Identify the blood parasite species.
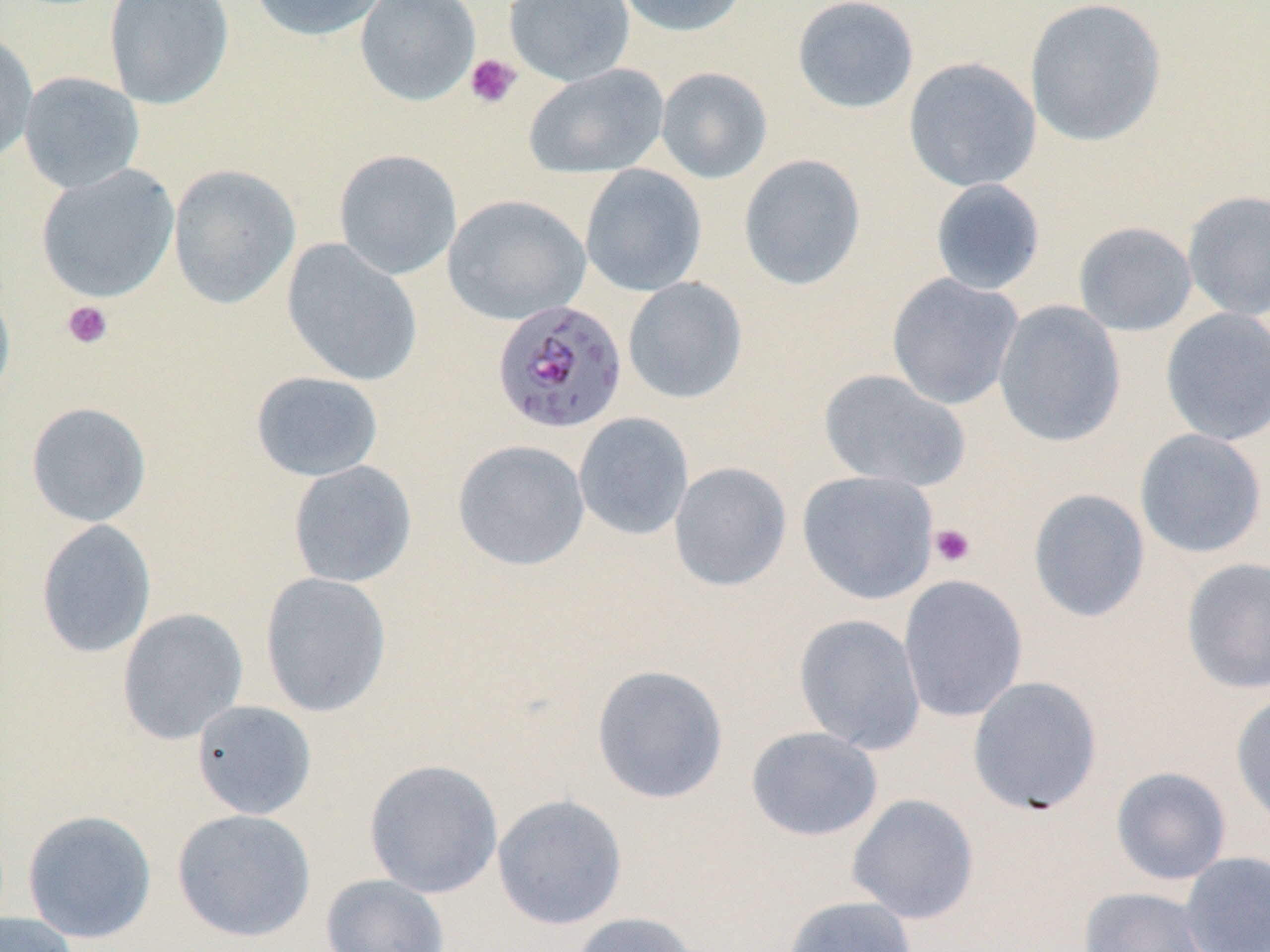

Plasmodium falciparum.

Summary:
  - Coordinate format: approximate bounding boxes as (x1, y1, x2, y2) in pixels
  - Plasmodium falciparum-infected red blood cell locations: (491, 299, 628, 435)
  - Platelet locations: (464, 53, 522, 109), (62, 300, 113, 349), (929, 523, 976, 568)
  - Uninfected red blood cell locations: (103, 0, 234, 110), (247, 0, 390, 42), (355, 0, 480, 105), (504, 0, 635, 86), (612, 0, 750, 37), (791, 0, 920, 115), (1024, 0, 1167, 148), (0, 29, 39, 164), (903, 57, 1041, 192), (523, 64, 669, 179), (656, 67, 773, 184), (19, 71, 145, 194), (333, 149, 462, 280), (738, 153, 867, 291), (36, 164, 179, 303), (168, 164, 301, 309), (580, 164, 707, 297), (929, 178, 1046, 295), (1182, 190, 1270, 321), (442, 194, 591, 325), (1073, 221, 1197, 336), (281, 239, 423, 386), (886, 273, 1024, 410), (623, 277, 748, 404), (0, 279, 16, 410), (993, 299, 1127, 448), (1160, 307, 1270, 446), (818, 368, 970, 492), (251, 370, 384, 482), (26, 401, 152, 527), (573, 412, 694, 540), (1134, 428, 1268, 559), (452, 439, 590, 571), (287, 460, 418, 588), (668, 462, 793, 592), (796, 470, 940, 604), (1027, 488, 1151, 623), (35, 519, 156, 658), (1181, 557, 1270, 695), (260, 572, 392, 718), (898, 574, 1028, 723), (117, 608, 249, 745), (793, 613, 926, 755), (591, 664, 729, 804), (967, 675, 1103, 815), (1230, 690, 1270, 830), (191, 700, 317, 819), (745, 726, 883, 841), (364, 758, 504, 898), (1110, 766, 1232, 885), (846, 793, 980, 924), (491, 794, 628, 930), (172, 808, 316, 943), (22, 809, 157, 943), (1180, 851, 1270, 952), (320, 873, 450, 952), (1078, 885, 1215, 952), (781, 895, 918, 952), (0, 912, 79, 952), (568, 912, 705, 952)
  - Modality: light microscopy
  - Stain: May-Grünwald-Giemsa
  - Image size: 1270×952 pixels
  - Field of view: single
  - Magnification: 1000x
  - Preparation: thin blood film